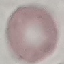

Summary:
  - Malaria status: uninfected
  - Preparation: thin smear
  - Capture: smartphone camera at the microscope eyepiece
  - Stain: Giemsa
  - Image type: cell patch, automatically extracted from a larger field of view and resized to 64 × 64 pixels